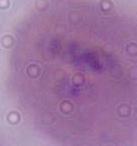 A red blood cell is shown. Micrograph. Captured at 1000x magnification.